Describe the morphology of the erythrocytes.
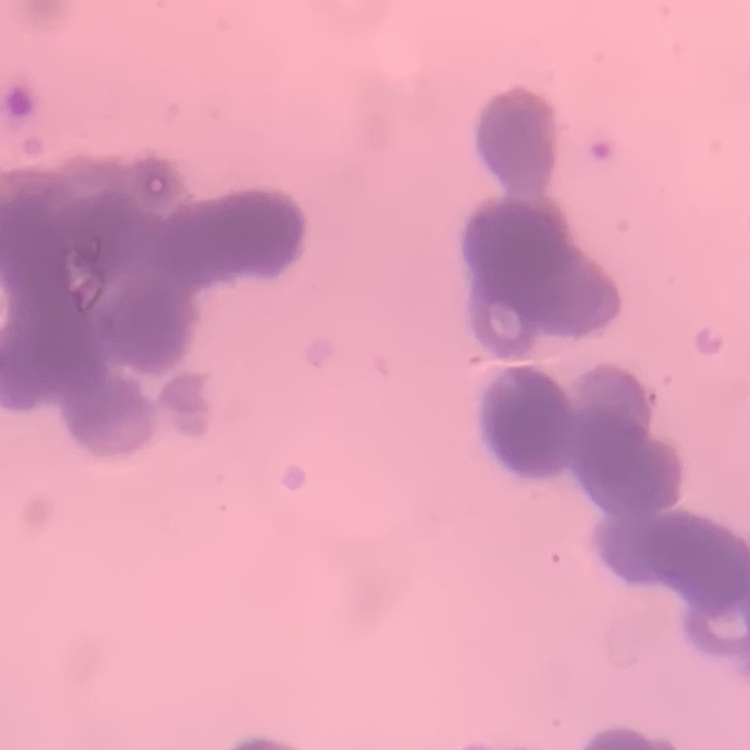
They show rouleaux formation.

Summary:
  - Preparation: thin peripheral smear
  - Image type: one tile cut from a larger photomicrograph
  - Stain: Field's or Giemsa